Identify the parasite.
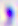

This is Toxoplasma gondii.

Micrograph. Captured at 400x magnification.